Comment on the morphology of the red blood cells.
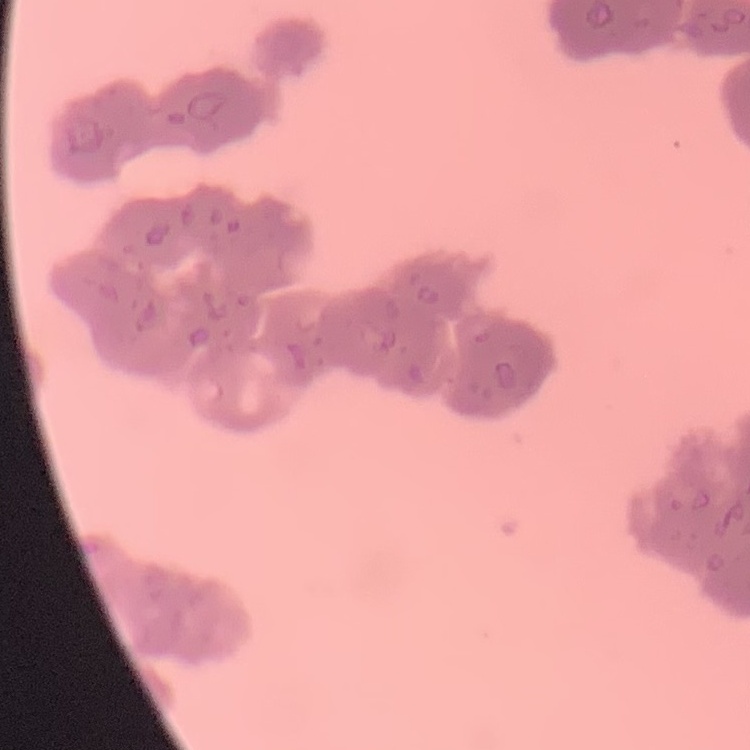

Rouleaux formation.

Summary:
  - Preparation: thin blood film
  - Stain: Field's or Giemsa
  - Image type: square crop of a larger photomicrograph